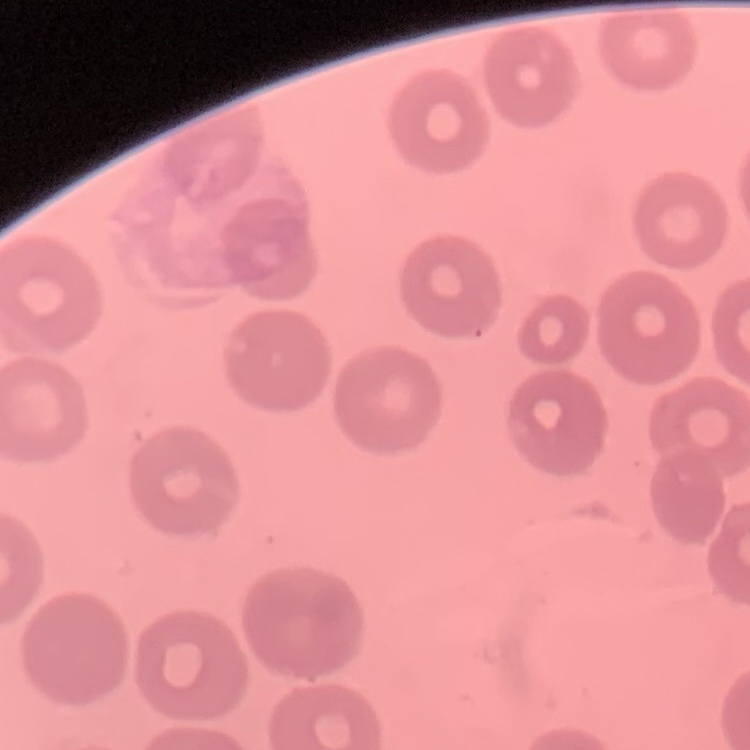
erythrocyte morphology = no rouleaux formation
stain = Field's or Giemsa
image type = one tile cut from a larger photomicrograph
preparation = thin blood film